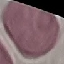

result = negative for malaria parasites
capture = smartphone camera at the microscope eyepiece
preparation = thin smear
stain = Giemsa
image type = automatically extracted cell patch, resized to 64 × 64 pixels